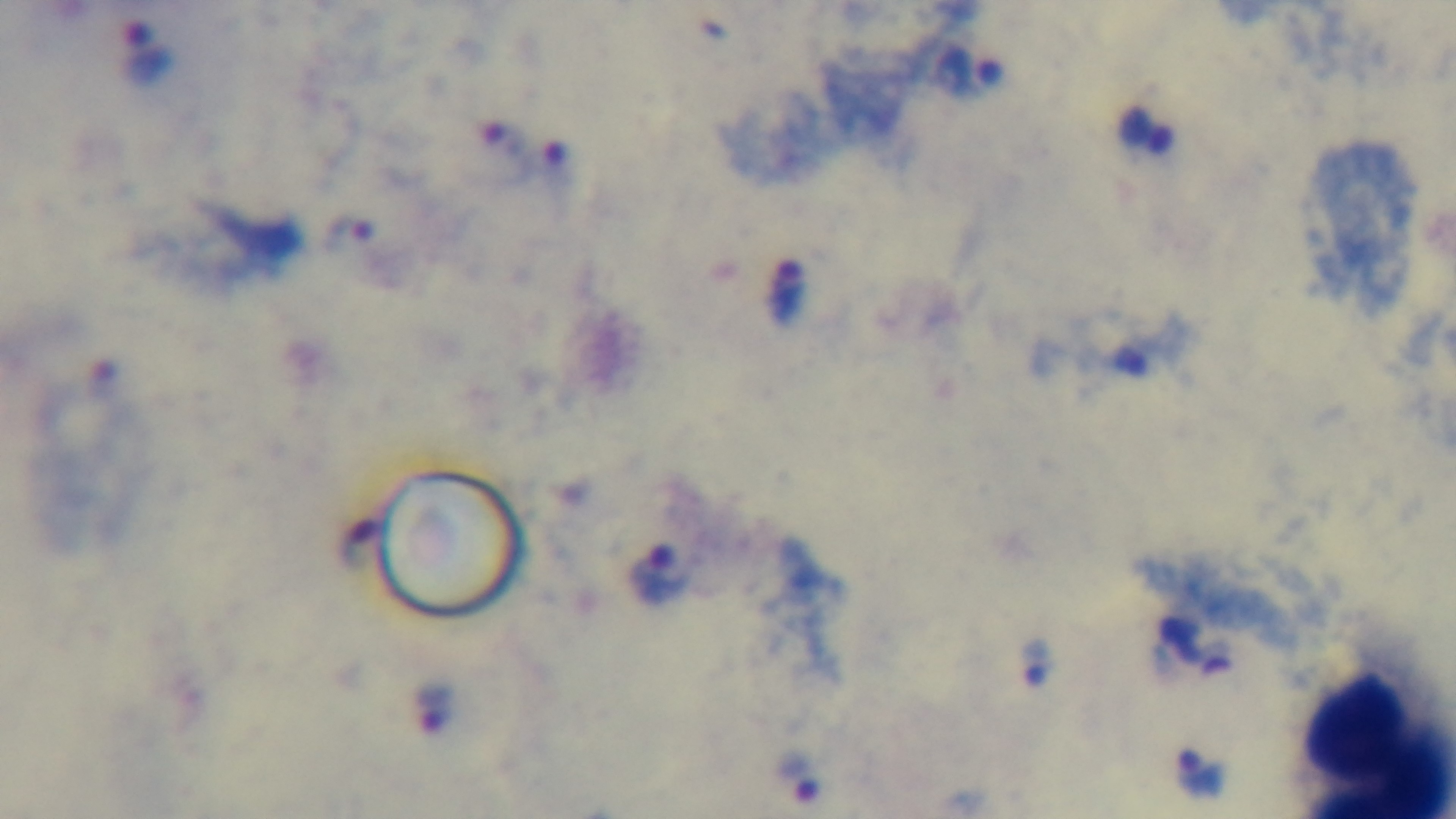
preparation = thick smear
modality = light microscopy
malaria status = positive
objective = 100x oil immersion
field of view = single
stain = Giemsa
capture = mounted 4K digital camera